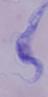
1000x magnification. Photomicrograph. A trypanosome is seen.